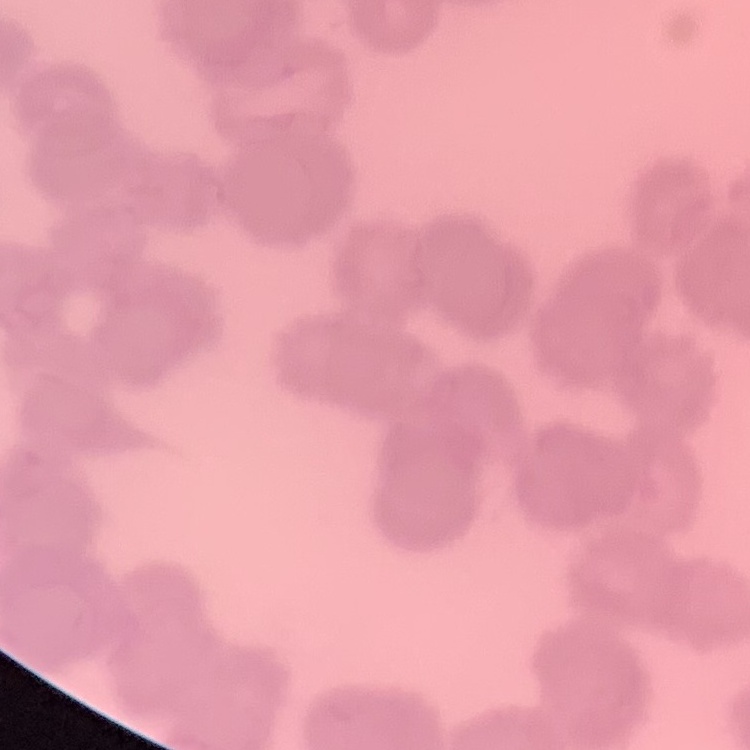 The red blood cells exhibit rouleaux formation. Thin peripheral smear. Field's or Giemsa stain. One tile cut from a larger photomicrograph.